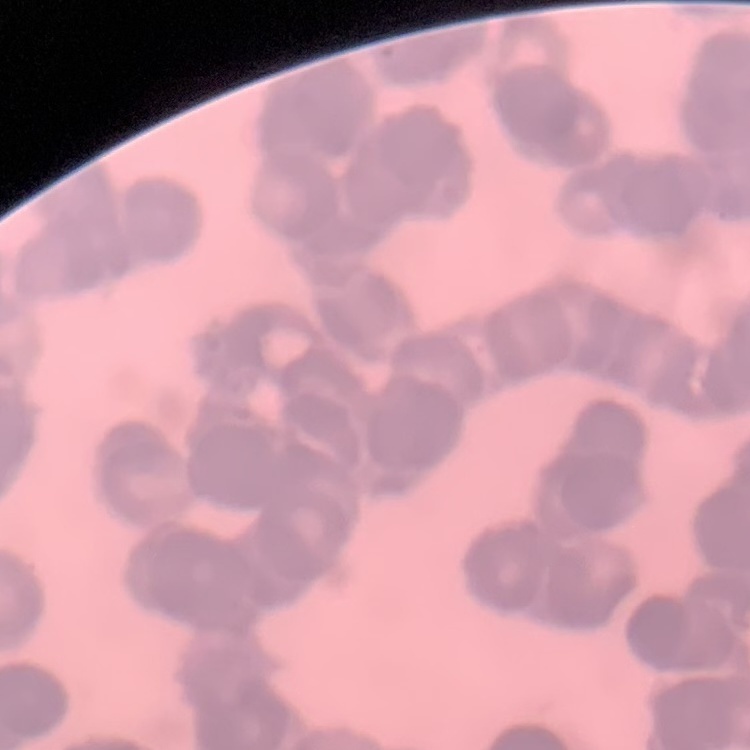
The erythrocytes show rouleaux formation. Square crop of a larger photomicrograph. Field's or Giemsa stain. Thin blood film.